State the preparation type.
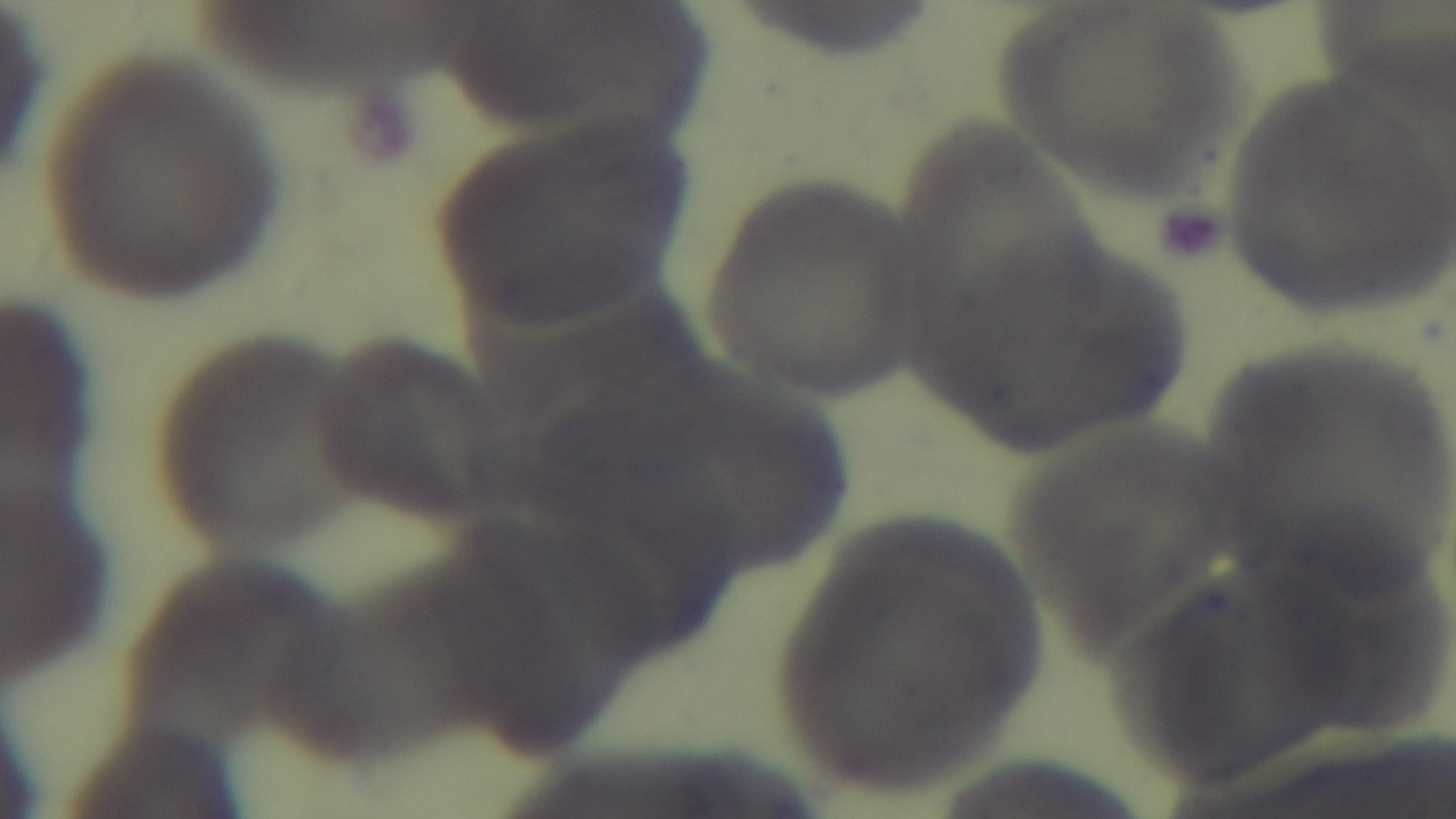

Thin.

modality = light microscopy
objective = 100x oil immersion
capture = mounted 4K digital camera
stain = Giemsa
malaria status = uninfected
field of view = single